State which parasite is depicted.
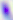
Toxoplasma gondii.

modality = photomicrograph
magnification = 400x